Locate and identify every blood parasite.
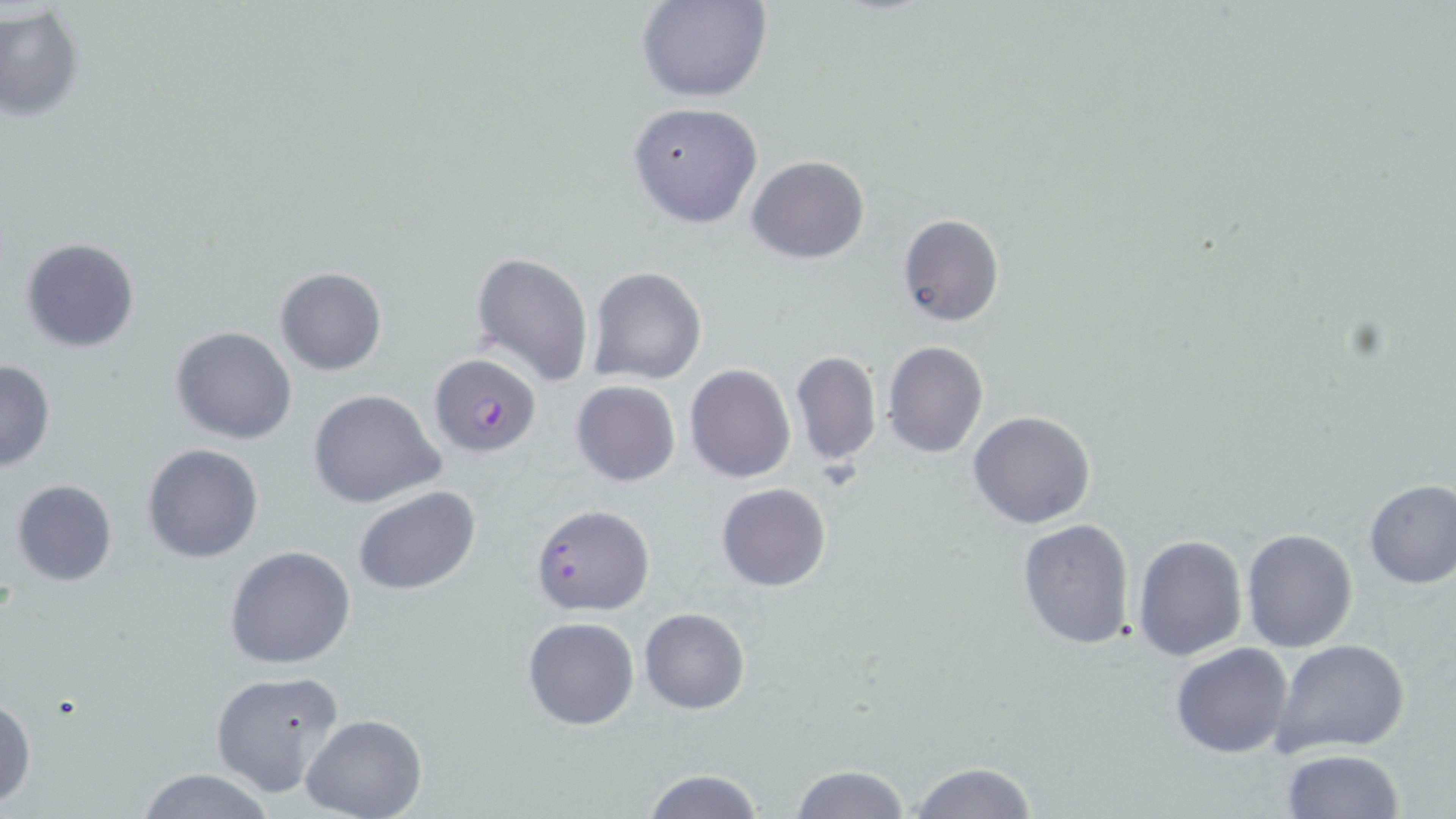

Approximate bounding boxes as named x1/y1/x2/y2 corners in pixels.
Plasmodium falciparum-infected red blood cells: (x1=429, y1=353, x2=541, y2=457).
No Plasmodium ovale, Plasmodium malariae, Plasmodium vivax, Babesia divergens, or Trypanosoma brucei observed.

Summary:
  - Uninfected red blood cell locations: (x1=638, y1=0, x2=771, y2=102), (x1=0, y1=5, x2=84, y2=120), (x1=627, y1=101, x2=763, y2=229), (x1=747, y1=155, x2=870, y2=263), (x1=896, y1=212, x2=1005, y2=328), (x1=20, y1=236, x2=141, y2=353), (x1=471, y1=251, x2=594, y2=387), (x1=275, y1=266, x2=386, y2=375), (x1=586, y1=266, x2=707, y2=385), (x1=170, y1=325, x2=297, y2=445), (x1=881, y1=340, x2=989, y2=458), (x1=789, y1=350, x2=882, y2=468), (x1=0, y1=359, x2=56, y2=473), (x1=685, y1=364, x2=795, y2=483), (x1=570, y1=379, x2=681, y2=487), (x1=307, y1=388, x2=446, y2=508), (x1=968, y1=410, x2=1097, y2=529), (x1=140, y1=442, x2=264, y2=564), (x1=1362, y1=478, x2=1456, y2=589), (x1=10, y1=480, x2=118, y2=588), (x1=716, y1=482, x2=831, y2=591), (x1=353, y1=487, x2=481, y2=596), (x1=531, y1=503, x2=656, y2=616), (x1=1018, y1=518, x2=1137, y2=651), (x1=1240, y1=528, x2=1358, y2=652), (x1=1132, y1=534, x2=1247, y2=661), (x1=224, y1=544, x2=356, y2=668), (x1=639, y1=607, x2=750, y2=713), (x1=522, y1=616, x2=639, y2=731), (x1=1270, y1=637, x2=1410, y2=757), (x1=1170, y1=642, x2=1293, y2=759), (x1=210, y1=670, x2=346, y2=798), (x1=0, y1=693, x2=36, y2=810), (x1=300, y1=715, x2=427, y2=819), (x1=1278, y1=749, x2=1405, y2=819), (x1=907, y1=761, x2=1040, y2=819), (x1=786, y1=764, x2=909, y2=819), (x1=135, y1=768, x2=276, y2=819), (x1=639, y1=769, x2=765, y2=819)
  - Slide-level diagnosis: Plasmodium falciparum
  - Image size: 1456×819 pixels
  - Magnification: 1000x
  - Field of view: one of a larger specimen
  - Preparation: thin blood film
  - Modality: light microscopy
  - Stain: May-Grünwald-Giemsa